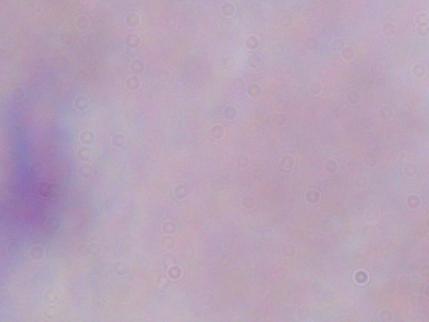
{
  "magnification": "1000x",
  "modality": "photomicrograph",
  "identification": "trypanosome"
}